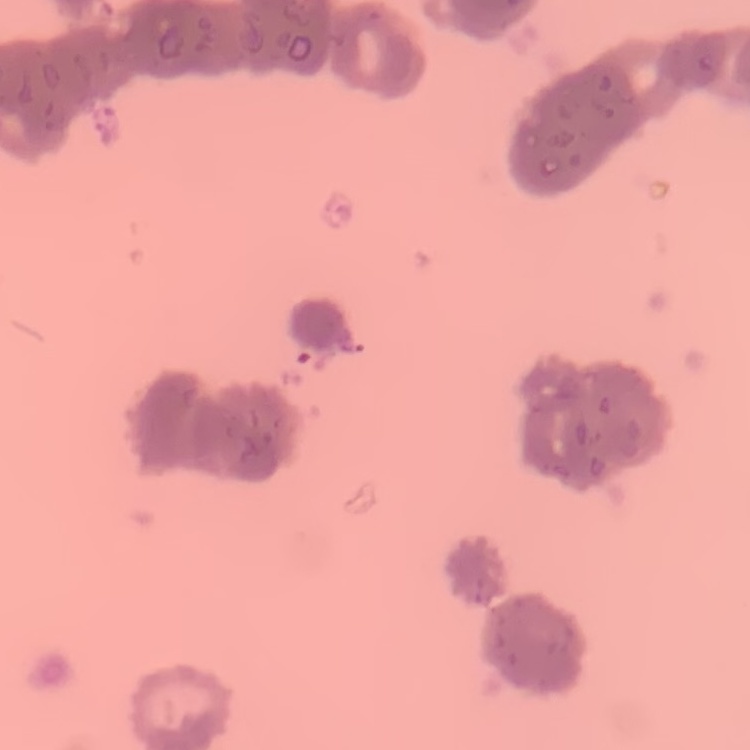
red blood cell morphology = rouleaux formation
preparation = thin peripheral smear
image type = one tile cut from a larger photomicrograph
stain = Field's or Giemsa